Classify this cell by malaria status.
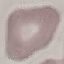

Uninfected.

Photographed with a smartphone camera at the microscope eyepiece. Giemsa-stained preparation. Thin smear of blood. Automatically extracted cell patch, resized to 64 × 64 pixels.